Classify this cell by malaria status.
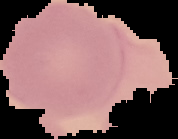

It is uninfected.

Summary:
  - Preparation: thin blood film
  - Image type: segmented cell region with the area outside set to black
  - Image size: 178×139 pixels